Assess the morphology of the erythrocytes.
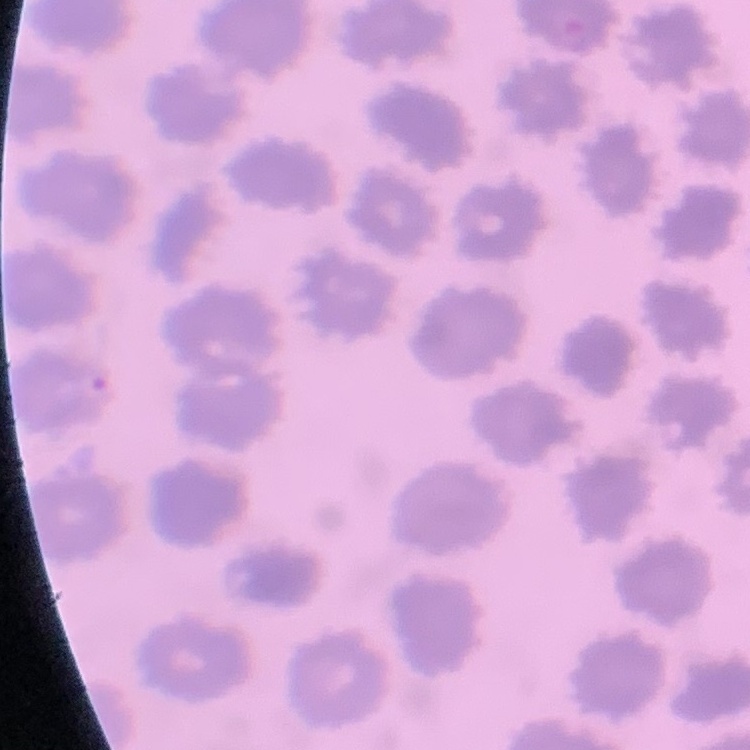

They show no rouleaux formation.

Summary:
  - Stain: Field's or Giemsa
  - Image type: square crop of a larger photomicrograph
  - Preparation: thin blood film